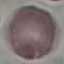

{
  "malaria_status": "uninfected",
  "preparation": "thin blood film",
  "image_type": "cell patch, automatically extracted from a larger field of view and resized to 64 × 64 pixels",
  "stain": "Giemsa",
  "capture": "smartphone through the microscope eyepiece"
}